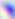

Toxoplasma gondii is shown. 400x magnification. Photomicrograph.